Name the parasite shown.
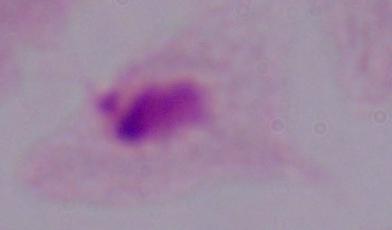
This is a trichomonad.

1000x magnification. Micrograph.